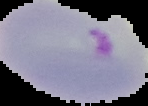
image size = 148×106 pixels
preparation = thin blood smear
malaria status = parasitized
image type = segmented cell region with the area outside set to black